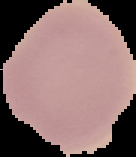
malaria status = uninfected
preparation = thin blood film
image type = cell region segmented out of the field of view; surrounding area masked to black
image size = 136×157 pixels